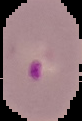
Summary:
  - Image type: segmented cell region on a black background
  - Preparation: thin blood film
  - Image size: 82×121 pixels
  - Malaria status: parasitized